Name the parasite shown.
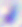
Toxoplasma gondii.

Summary:
  - Magnification: 400x
  - Modality: photomicrograph